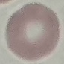

Summary:
  - Result: no malaria parasites detected
  - Capture: smartphone camera at the microscope eyepiece
  - Preparation: thin blood smear
  - Image type: automatically extracted cell patch, resized to 64 × 64 pixels
  - Stain: Giemsa